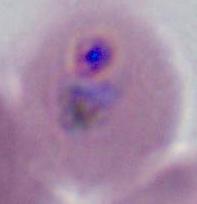
Summary:
  - Identification: Plasmodium
  - Modality: micrograph
  - Magnification: 400x or 1000x